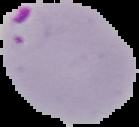
preparation = thin blood smear
image type = segmented cell region on a black background
image size = 139×127 pixels
result = malaria parasites detected